Identify the parasite.
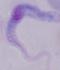
This is a trypanosome.

1000x magnification. Photomicrograph.